Classify this cell by malaria status.
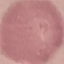
It is uninfected.

Cell patch, automatically extracted from a larger field of view and resized to 64 × 64 pixels. Photographed with a smartphone camera at the microscope eyepiece. Thin smear of blood. Giemsa-stained preparation.